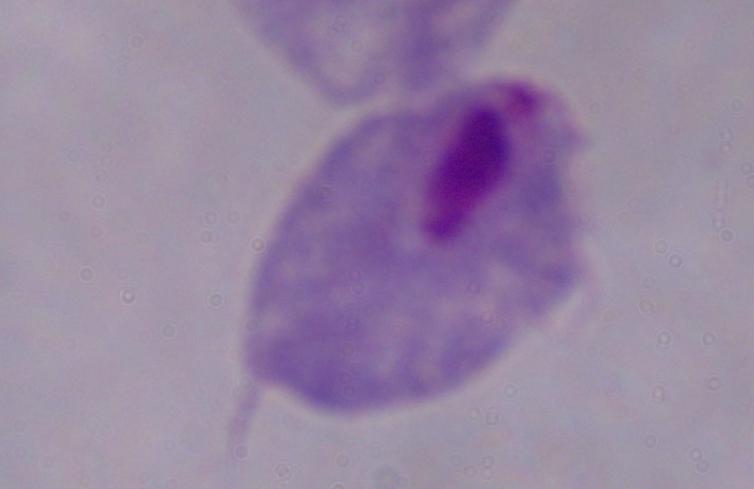

Photomicrograph. A trichomonad is shown. Captured at 1000x magnification.